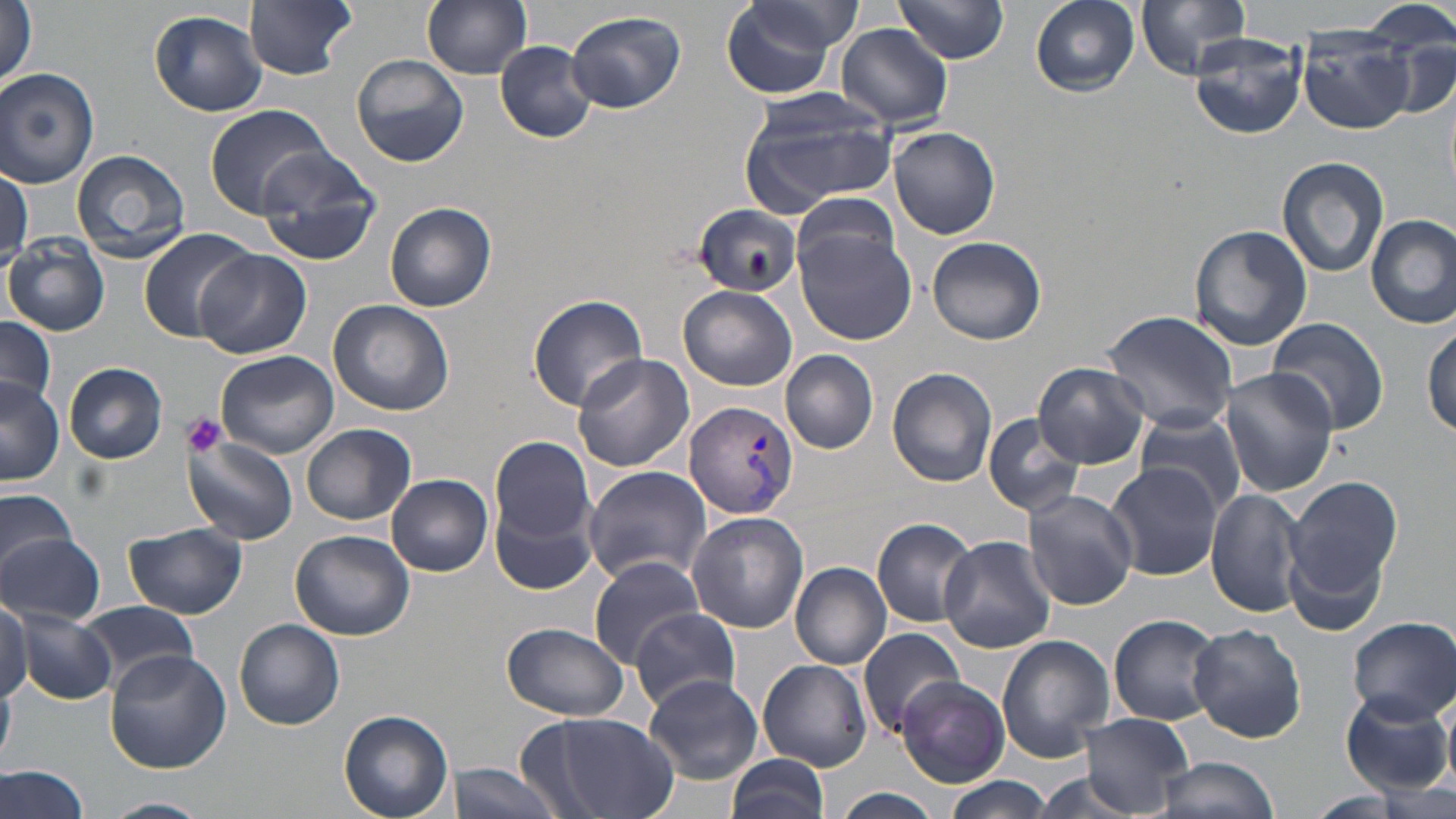

Approximate bounding boxes as named x1/y1/x2/y2 corners in pixels. Platelet locations: (x1=183, y1=412, x2=228, y2=456). Uninfected red blood cell locations: (x1=244, y1=0, x2=359, y2=79), (x1=421, y1=0, x2=533, y2=78), (x1=720, y1=0, x2=855, y2=99), (x1=1030, y1=0, x2=1140, y2=95), (x1=1138, y1=0, x2=1249, y2=78), (x1=1, y1=2, x2=37, y2=91), (x1=894, y1=2, x2=1010, y2=66), (x1=1363, y1=2, x2=1456, y2=55), (x1=150, y1=9, x2=268, y2=117), (x1=567, y1=11, x2=687, y2=113), (x1=836, y1=25, x2=954, y2=129), (x1=1296, y1=28, x2=1416, y2=134), (x1=1380, y1=29, x2=1455, y2=117), (x1=1189, y1=33, x2=1305, y2=140), (x1=495, y1=41, x2=598, y2=143), (x1=352, y1=52, x2=470, y2=168), (x1=0, y1=67, x2=99, y2=188), (x1=738, y1=88, x2=901, y2=214), (x1=204, y1=104, x2=337, y2=219), (x1=889, y1=126, x2=1001, y2=240), (x1=253, y1=145, x2=382, y2=266), (x1=71, y1=148, x2=193, y2=260), (x1=1277, y1=156, x2=1388, y2=278), (x1=0, y1=165, x2=30, y2=269), (x1=792, y1=190, x2=906, y2=282), (x1=385, y1=202, x2=497, y2=313), (x1=690, y1=202, x2=802, y2=298), (x1=1365, y1=215, x2=1456, y2=329), (x1=1190, y1=224, x2=1314, y2=351), (x1=138, y1=228, x2=257, y2=341), (x1=796, y1=230, x2=916, y2=346), (x1=5, y1=235, x2=110, y2=337), (x1=926, y1=236, x2=1046, y2=345), (x1=194, y1=249, x2=309, y2=359), (x1=678, y1=286, x2=798, y2=392), (x1=527, y1=293, x2=648, y2=411), (x1=328, y1=300, x2=456, y2=418), (x1=1101, y1=311, x2=1239, y2=432), (x1=0, y1=315, x2=58, y2=416), (x1=1267, y1=319, x2=1389, y2=436), (x1=1424, y1=322, x2=1456, y2=441), (x1=215, y1=350, x2=339, y2=460), (x1=781, y1=350, x2=878, y2=453), (x1=571, y1=352, x2=694, y2=471), (x1=1032, y1=361, x2=1152, y2=469), (x1=62, y1=362, x2=169, y2=464), (x1=887, y1=367, x2=998, y2=487), (x1=1219, y1=368, x2=1341, y2=498), (x1=0, y1=378, x2=64, y2=486), (x1=1134, y1=410, x2=1245, y2=515), (x1=982, y1=411, x2=1090, y2=516), (x1=302, y1=423, x2=416, y2=524), (x1=490, y1=436, x2=597, y2=552), (x1=185, y1=437, x2=298, y2=545), (x1=1104, y1=462, x2=1222, y2=582), (x1=582, y1=465, x2=712, y2=587), (x1=387, y1=476, x2=493, y2=576), (x1=1281, y1=476, x2=1405, y2=626), (x1=489, y1=483, x2=598, y2=596), (x1=1205, y1=488, x2=1305, y2=616), (x1=0, y1=489, x2=80, y2=575), (x1=1022, y1=489, x2=1139, y2=611), (x1=685, y1=511, x2=809, y2=634), (x1=872, y1=517, x2=979, y2=628), (x1=122, y1=523, x2=248, y2=618), (x1=289, y1=530, x2=415, y2=641), (x1=0, y1=531, x2=105, y2=627), (x1=938, y1=534, x2=1057, y2=653), (x1=588, y1=555, x2=704, y2=667), (x1=791, y1=563, x2=892, y2=669), (x1=0, y1=596, x2=31, y2=705), (x1=79, y1=601, x2=199, y2=691), (x1=630, y1=607, x2=738, y2=711), (x1=15, y1=611, x2=114, y2=705), (x1=1108, y1=613, x2=1224, y2=727), (x1=1348, y1=617, x2=1456, y2=723), (x1=234, y1=618, x2=346, y2=731), (x1=501, y1=622, x2=629, y2=721), (x1=1188, y1=625, x2=1305, y2=744), (x1=858, y1=627, x2=966, y2=736), (x1=995, y1=634, x2=1114, y2=765), (x1=106, y1=650, x2=231, y2=774), (x1=756, y1=658, x2=872, y2=771), (x1=641, y1=673, x2=763, y2=784), (x1=895, y1=676, x2=1010, y2=786), (x1=0, y1=680, x2=13, y2=766), (x1=1342, y1=691, x2=1451, y2=797), (x1=526, y1=709, x2=679, y2=819), (x1=339, y1=710, x2=453, y2=819), (x1=1081, y1=712, x2=1194, y2=815), (x1=724, y1=755, x2=830, y2=819), (x1=1152, y1=755, x2=1281, y2=819), (x1=449, y1=761, x2=566, y2=819), (x1=0, y1=765, x2=95, y2=819), (x1=941, y1=776, x2=1057, y2=819), (x1=835, y1=788, x2=941, y2=819), (x1=101, y1=797, x2=211, y2=819). Plasmodium vivax-infected red blood cell locations: (x1=684, y1=400, x2=798, y2=520). Slide-level diagnosis: Plasmodium vivax. Optical microscopy. May-Grünwald-Giemsa-stained preparation. One field of a larger specimen. Thin blood film. Captured at 1000x magnification. Image is 1456×819 pixels.